Name the blood parasite species.
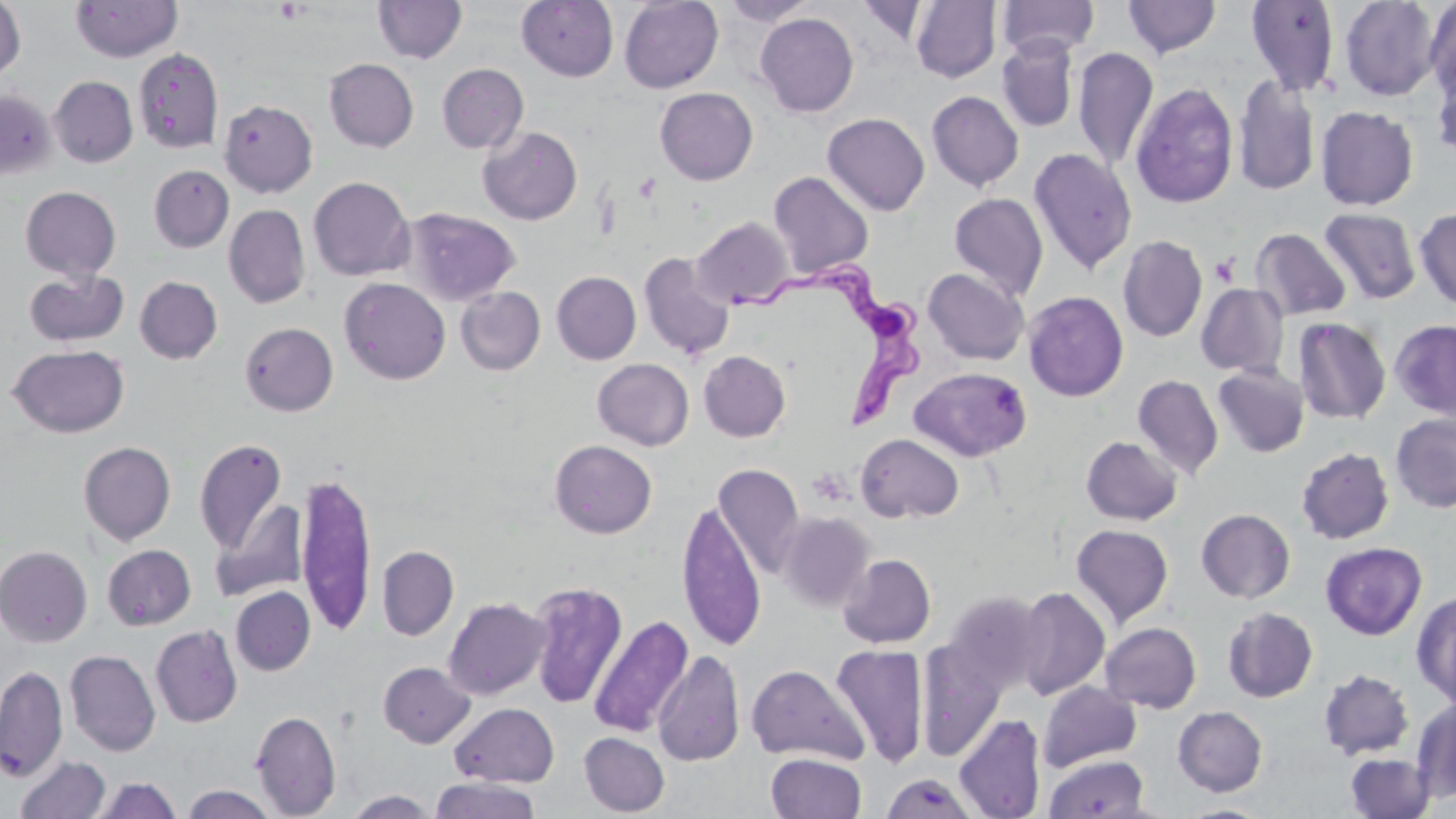

Trypanosoma brucei.

Approximate bounding boxes as [x1, y1, x2, y2] in pixels. Platelet locations: [274, 1, 306, 24], [1209, 253, 1240, 287]. Uninfected red blood cell locations: [71, 0, 182, 62], [721, 0, 818, 26], [1123, 0, 1222, 58], [1339, 0, 1441, 101], [0, 1, 26, 83], [373, 1, 467, 64], [516, 1, 618, 82], [619, 1, 723, 93], [855, 1, 932, 46], [910, 1, 1002, 83], [997, 1, 1099, 57], [1245, 1, 1341, 95], [1424, 1, 1456, 102], [755, 13, 858, 117], [996, 38, 1078, 133], [1073, 46, 1158, 172], [133, 47, 224, 154], [323, 58, 419, 152], [1431, 61, 1456, 163], [437, 63, 528, 153], [49, 76, 138, 168], [1233, 76, 1320, 196], [1131, 80, 1238, 209], [655, 87, 758, 185], [0, 89, 56, 182], [926, 91, 1024, 191], [219, 99, 318, 197], [1315, 106, 1418, 210], [823, 113, 930, 216], [478, 126, 582, 225], [1028, 148, 1137, 275], [148, 165, 234, 252], [768, 171, 874, 278], [308, 176, 415, 282], [20, 186, 121, 281], [949, 192, 1048, 302], [223, 204, 311, 308], [401, 207, 521, 306], [1319, 207, 1422, 305], [1415, 207, 1456, 309], [692, 217, 793, 308], [1250, 228, 1351, 322], [1117, 235, 1207, 343], [639, 252, 735, 359], [922, 268, 1030, 365], [24, 269, 129, 347], [552, 271, 641, 364], [134, 276, 223, 364], [339, 277, 450, 384], [1196, 283, 1289, 377], [456, 286, 545, 375], [1023, 291, 1128, 401], [1292, 317, 1391, 425], [1390, 319, 1456, 419], [239, 322, 338, 416], [6, 344, 130, 438], [698, 350, 790, 442], [593, 358, 693, 450], [1213, 364, 1310, 457], [909, 367, 1032, 461], [1133, 374, 1224, 480], [1390, 413, 1456, 513], [855, 433, 964, 523], [1081, 436, 1182, 525], [194, 437, 288, 555], [549, 439, 657, 538], [78, 441, 176, 545], [1296, 447, 1394, 544], [713, 464, 805, 578], [295, 470, 378, 637], [676, 499, 766, 651], [212, 500, 308, 602], [1196, 509, 1295, 603], [777, 511, 874, 612], [1070, 524, 1174, 628], [1320, 542, 1427, 640], [102, 544, 196, 630], [0, 545, 92, 647], [377, 545, 458, 641], [838, 554, 936, 648], [526, 581, 628, 709], [230, 587, 315, 676], [1014, 587, 1111, 700], [1412, 590, 1456, 706], [940, 592, 1045, 695], [443, 596, 550, 700], [1222, 607, 1318, 703], [588, 615, 693, 738], [1100, 622, 1201, 713], [150, 624, 243, 728], [916, 638, 1006, 760], [830, 645, 930, 766], [652, 649, 745, 768], [65, 650, 161, 756], [378, 661, 476, 748], [0, 664, 68, 781], [746, 664, 868, 765], [1318, 669, 1414, 760], [1037, 681, 1142, 771], [1411, 699, 1456, 803], [449, 702, 559, 786], [1172, 706, 1268, 796], [250, 710, 341, 818], [954, 714, 1045, 819], [579, 732, 669, 816], [766, 752, 867, 819], [1344, 752, 1435, 818], [15, 755, 112, 818], [1044, 755, 1149, 818], [91, 776, 182, 818], [883, 776, 981, 819], [428, 777, 542, 819], [180, 784, 280, 819], [344, 789, 438, 818], [1179, 803, 1272, 818]. Trypanosoma brucei locations: [721, 263, 925, 435]. May-Grünwald-Giemsa stain. Captured at 1000x magnification. One field of a larger specimen. Image is 1456×819 pixels. Thin blood film. Light microscopy.